Report the malaria status of this cell.
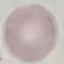

It is uninfected.

{
  "stain": "Giemsa",
  "image_type": "cell patch, automatically extracted from a larger field of view and resized to 64 × 64 pixels",
  "preparation": "thin blood film",
  "capture": "smartphone through the microscope eyepiece"
}